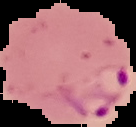

preparation = thin blood smear
image type = cell region segmented out of the field of view; surrounding area masked to black
image size = 136×127 pixels
result = malaria parasites detected